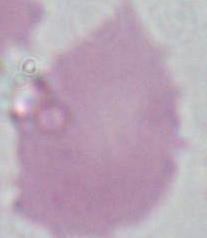
Micrograph. Captured at 1000x magnification. An erythrocyte is seen.